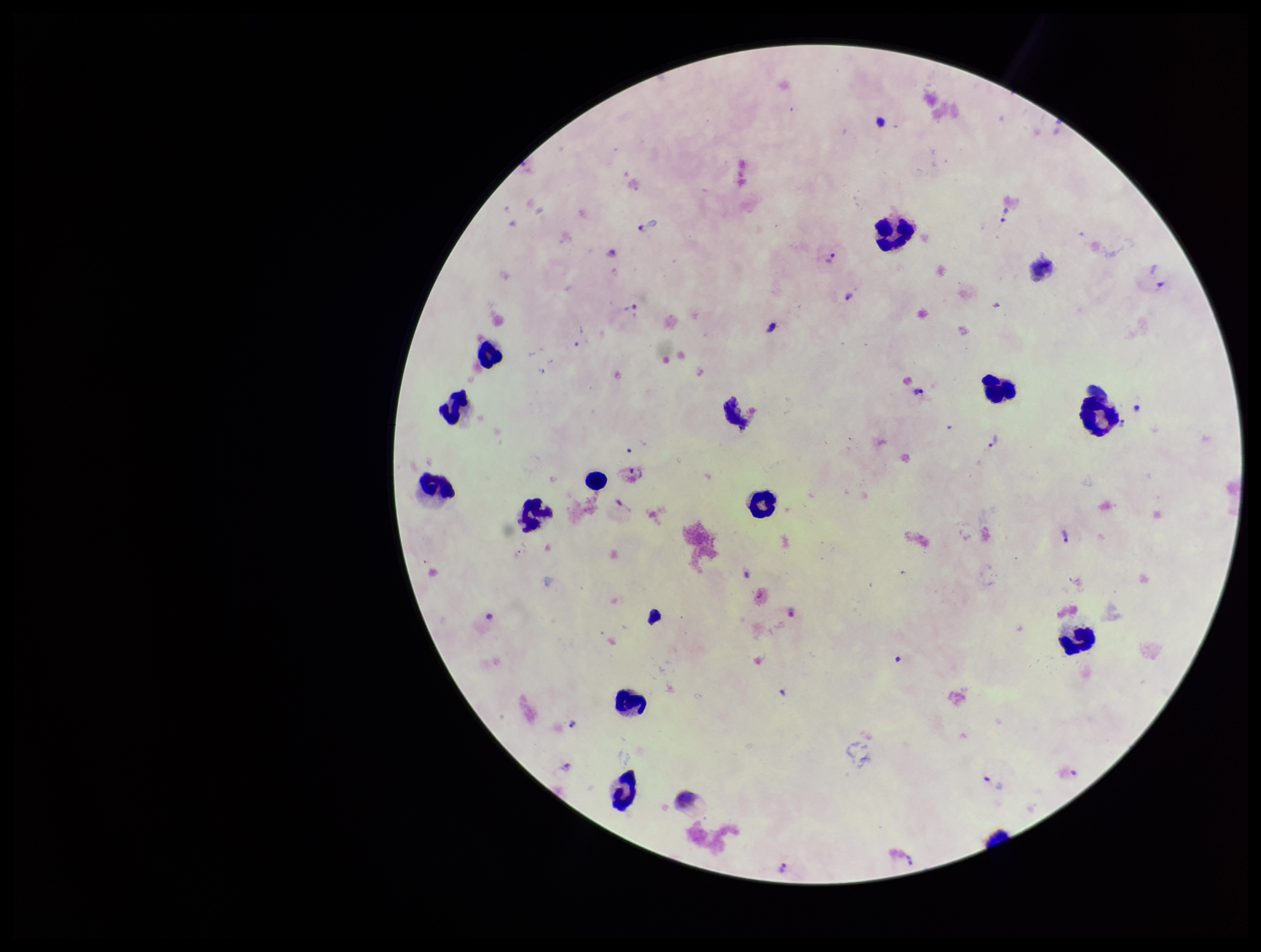
{
  "species_reported_for_this_patient": "Plasmodium vivax",
  "patient_malaria_status": "infected",
  "leukocyte_count": 13,
  "image_size": "1261×952 pixels",
  "capture": "smartphone photograph through the microscope eyepiece",
  "plasmodium_parasites": "seen",
  "field_of_view": "single",
  "preparation": "thick smear",
  "stain": "Giemsa",
  "parasite_count": 16
}